Report the malaria status of this cell.
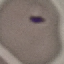
It is uninfected.

Summary:
  - Stain: Giemsa
  - Preparation: thin blood smear
  - Image type: cell patch, automatically extracted from a larger field of view and resized to 64 × 64 pixels
  - Capture: smartphone camera at the microscope eyepiece